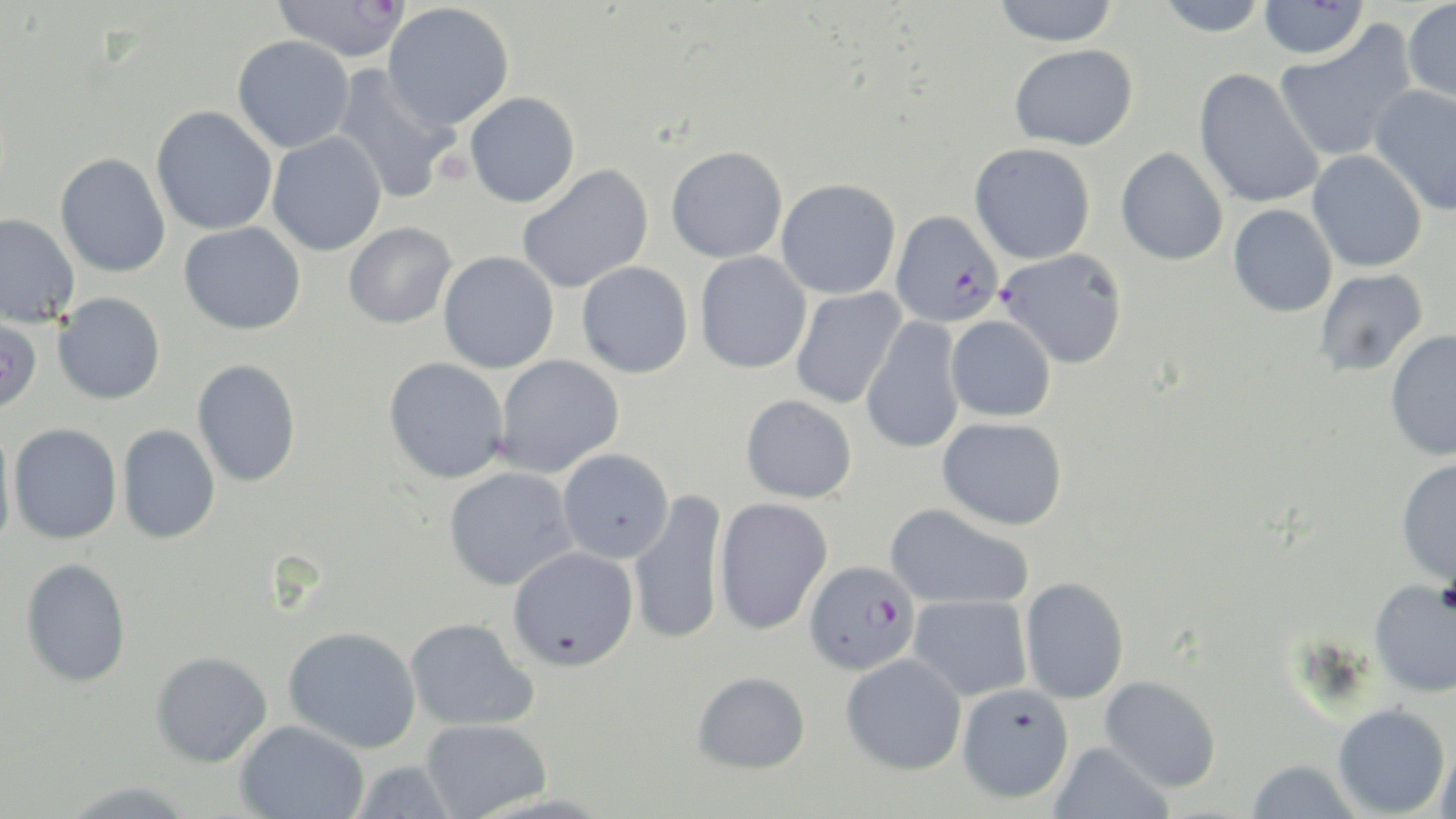 Approximate bounding boxes as named x1/y1/x2/y2 corners in pixels. Plasmodium falciparum-infected red blood cell locations: (x1=891, y1=210, x2=1004, y2=327), (x1=803, y1=561, x2=918, y2=676). Platelet locations: (x1=433, y1=149, x2=474, y2=184). Uninfected red blood cell locations: (x1=994, y1=0, x2=1119, y2=47), (x1=1155, y1=0, x2=1268, y2=37), (x1=272, y1=1, x2=411, y2=62), (x1=1258, y1=1, x2=1368, y2=59), (x1=1403, y1=1, x2=1456, y2=105), (x1=382, y1=3, x2=514, y2=131), (x1=1274, y1=21, x2=1417, y2=164), (x1=232, y1=35, x2=354, y2=153), (x1=1009, y1=44, x2=1138, y2=150), (x1=331, y1=65, x2=460, y2=204), (x1=1194, y1=68, x2=1325, y2=209), (x1=1370, y1=85, x2=1456, y2=215), (x1=464, y1=92, x2=580, y2=207), (x1=151, y1=106, x2=277, y2=235), (x1=267, y1=132, x2=387, y2=256), (x1=969, y1=142, x2=1096, y2=264), (x1=666, y1=145, x2=788, y2=263), (x1=1115, y1=147, x2=1228, y2=265), (x1=1307, y1=150, x2=1427, y2=273), (x1=55, y1=153, x2=171, y2=277), (x1=516, y1=164, x2=654, y2=294), (x1=776, y1=179, x2=901, y2=299), (x1=1228, y1=204, x2=1337, y2=317), (x1=0, y1=213, x2=80, y2=329), (x1=178, y1=222, x2=305, y2=334), (x1=344, y1=222, x2=456, y2=328), (x1=998, y1=248, x2=1128, y2=368), (x1=438, y1=251, x2=559, y2=374), (x1=694, y1=251, x2=812, y2=374), (x1=577, y1=261, x2=693, y2=378), (x1=1314, y1=269, x2=1428, y2=377), (x1=790, y1=288, x2=906, y2=409), (x1=53, y1=292, x2=165, y2=404), (x1=0, y1=313, x2=43, y2=413), (x1=945, y1=315, x2=1056, y2=422), (x1=862, y1=316, x2=965, y2=455), (x1=1384, y1=329, x2=1456, y2=461), (x1=493, y1=355, x2=624, y2=477), (x1=384, y1=357, x2=509, y2=483), (x1=192, y1=359, x2=301, y2=487), (x1=741, y1=394, x2=857, y2=503), (x1=937, y1=417, x2=1067, y2=530), (x1=8, y1=422, x2=122, y2=544), (x1=117, y1=424, x2=221, y2=544), (x1=0, y1=425, x2=17, y2=557), (x1=557, y1=448, x2=674, y2=563), (x1=1395, y1=459, x2=1456, y2=585), (x1=443, y1=467, x2=578, y2=591), (x1=629, y1=490, x2=728, y2=646), (x1=713, y1=497, x2=833, y2=635), (x1=885, y1=503, x2=1034, y2=609), (x1=508, y1=546, x2=639, y2=671), (x1=20, y1=557, x2=132, y2=687), (x1=1019, y1=577, x2=1129, y2=704), (x1=1368, y1=578, x2=1456, y2=698), (x1=908, y1=594, x2=1032, y2=701), (x1=404, y1=618, x2=538, y2=732), (x1=283, y1=626, x2=421, y2=753), (x1=150, y1=651, x2=272, y2=768), (x1=840, y1=652, x2=967, y2=775), (x1=692, y1=671, x2=810, y2=773), (x1=1099, y1=676, x2=1221, y2=791), (x1=956, y1=683, x2=1074, y2=803), (x1=1333, y1=703, x2=1450, y2=817), (x1=421, y1=719, x2=551, y2=818), (x1=235, y1=720, x2=369, y2=818), (x1=1436, y1=741, x2=1456, y2=819), (x1=1048, y1=742, x2=1173, y2=819), (x1=1245, y1=759, x2=1361, y2=819), (x1=348, y1=760, x2=460, y2=819), (x1=60, y1=780, x2=199, y2=819). Slide-level diagnosis: Plasmodium falciparum. Single field of view. 1000x magnification. Light microscopy. Image is 1456×819 pixels. May-Grünwald-Giemsa stain. Thin blood smear.